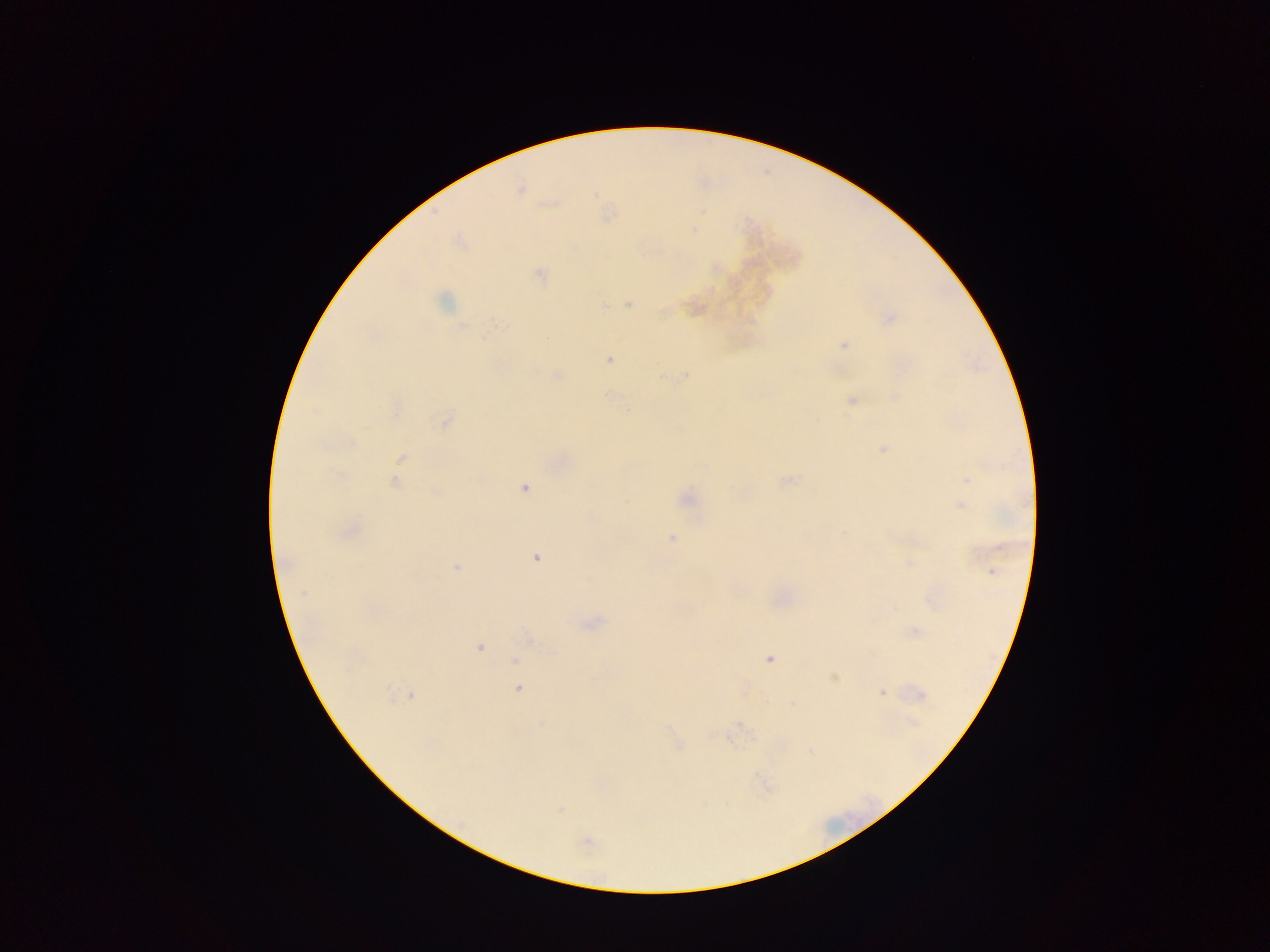
Approximate centers as x y in pixels.
Summary:
  - Plasmodium parasite locations: 520 189; 693 229; 539 273; 444 301; 630 303; 604 306; 890 318; 462 325; 844 345; 609 359; 558 374; 684 375; 895 397; 852 400; 398 408; 445 422; 884 448; 401 458; 787 480; 967 480; 394 482; 524 488; 437 492; 687 499; 961 506; 843 533; 671 538; 535 558; 909 564; 456 567; 992 572; 302 594; 915 632; 479 647; 769 659; 515 660; 834 678; 518 689; 882 692; 389 693; 410 695; 921 695; 913 722; 542 724; 679 746; 559 809; 587 843
  - Preparation: thick blood smear
  - Image size: 1270×952 pixels
  - Field of view: single
  - Capture: mobile-phone photograph through a microscope
  - Country: Ghana